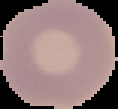

Summary:
  - Image type: segmented cell region with the area outside set to black
  - Image size: 118×109 pixels
  - Preparation: thin blood film
  - Result: no Plasmodium parasites detected